Assess the morphology of the red blood cells.
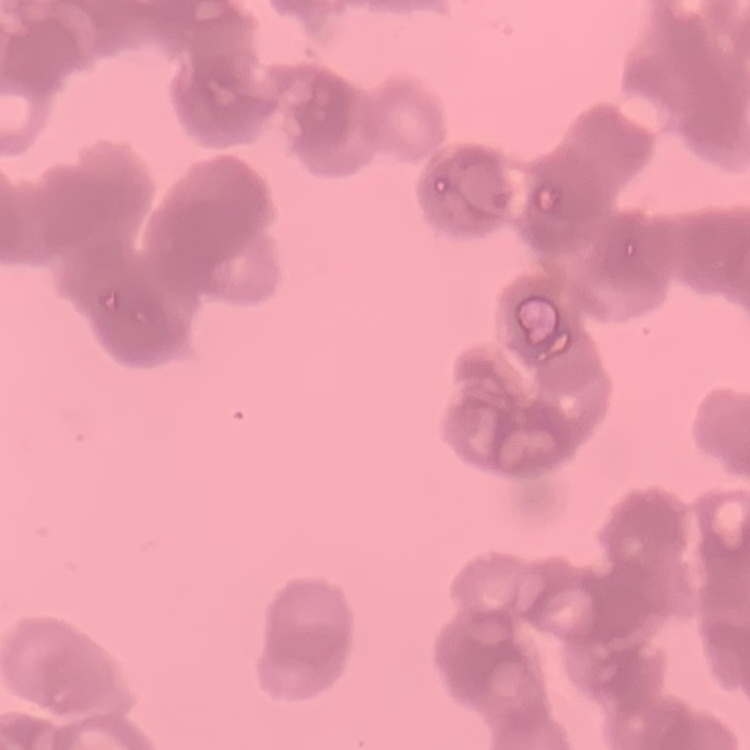

They show rouleaux formation.

Summary:
  - Preparation: thin blood film
  - Stain: Field's or Giemsa
  - Image type: one tile cut from a larger photomicrograph